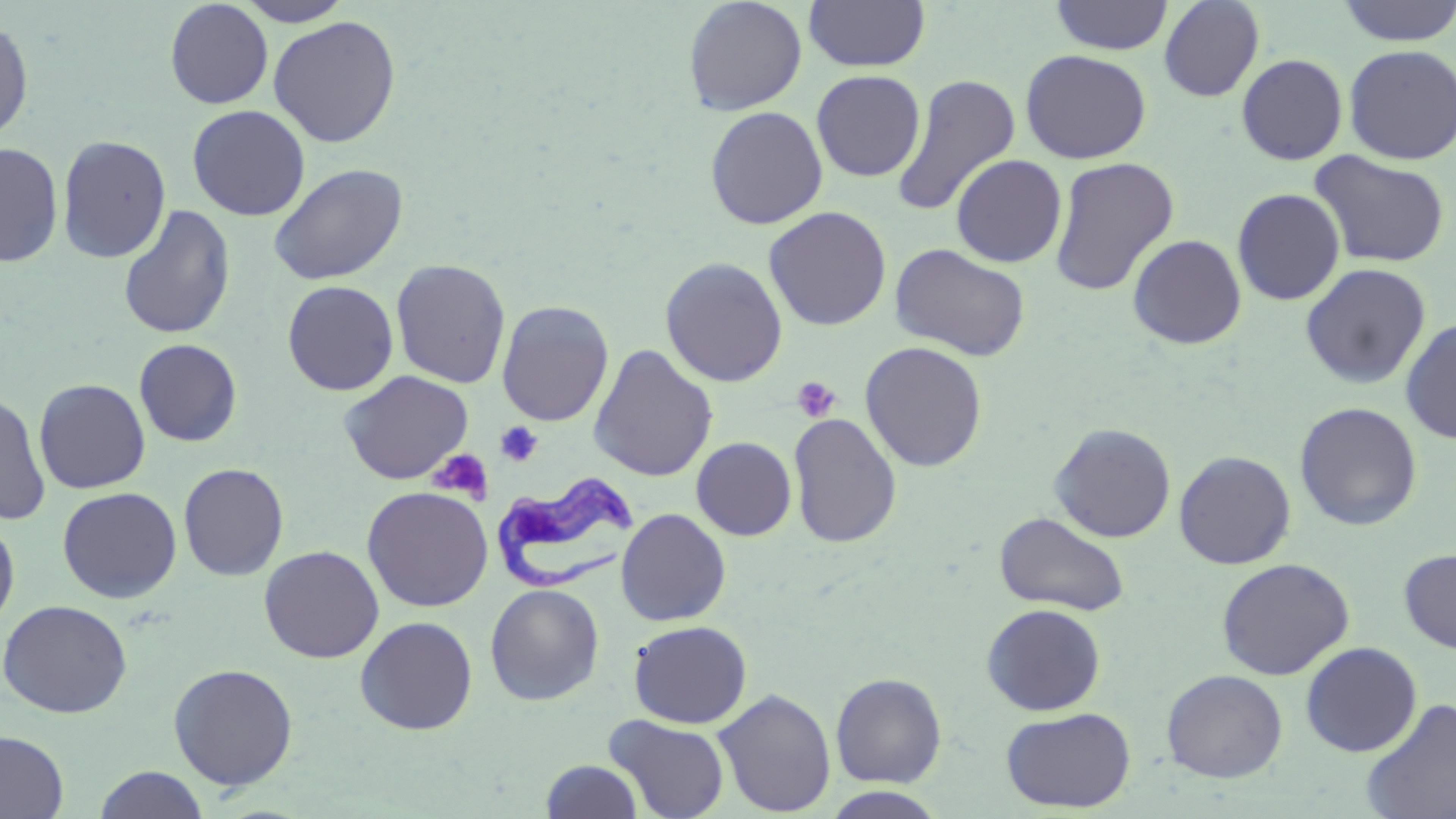

Summary:
  - Coordinate format: approximate bounding boxes as (x1,y1)-(x2,y2) corner pairs in pixels
  - Trypanosoma brucei locations: (490,469)-(639,593)
  - Uninfected red blood cell locations: (236,0)-(354,26), (683,0)-(807,116), (803,0)-(930,72), (1050,0)-(1174,56), (1158,0)-(1265,102), (1335,0)-(1456,47), (165,1)-(273,109), (268,15)-(401,148), (0,16)-(34,144), (1343,43)-(1456,165), (1020,49)-(1152,163), (1236,53)-(1348,165), (811,70)-(925,182), (892,73)-(1020,217), (187,105)-(311,221), (705,105)-(828,230), (57,134)-(171,263), (0,142)-(63,268), (1309,151)-(1451,268), (951,154)-(1067,267), (1049,157)-(1179,296), (269,163)-(408,286), (1232,188)-(1345,305), (117,205)-(235,341), (764,206)-(892,331), (1127,233)-(1247,349), (889,243)-(1030,361), (660,257)-(788,387), (391,259)-(511,388), (1300,263)-(1431,389), (282,280)-(399,396), (497,300)-(614,426), (1400,317)-(1456,444), (133,339)-(242,447), (860,341)-(988,472), (588,344)-(719,482), (339,370)-(473,485), (34,378)-(151,494), (0,391)-(51,525), (1294,402)-(1422,531), (788,412)-(902,548), (1049,422)-(1176,542), (692,437)-(796,540), (1174,450)-(1296,569), (178,462)-(289,581), (362,486)-(493,611), (57,487)-(182,603), (615,508)-(731,626), (994,512)-(1130,617), (0,517)-(20,634), (259,545)-(384,663), (1399,547)-(1456,653), (1216,557)-(1354,680), (485,583)-(605,705), (0,599)-(133,718), (981,603)-(1106,715), (355,616)-(477,735), (628,620)-(752,728), (1300,642)-(1422,757), (168,662)-(298,791), (1162,669)-(1288,782), (830,672)-(947,788), (713,688)-(836,817), (1360,698)-(1456,819), (1001,707)-(1136,813), (604,715)-(730,819), (0,730)-(69,818), (541,759)-(644,818), (93,766)-(210,819), (823,787)-(949,819)
  - Platelet locations: (792,376)-(841,423), (495,421)-(543,467), (428,449)-(494,504)
  - Slide-level diagnosis: Trypanosoma brucei
  - Stain: May-Grünwald-Giemsa
  - Modality: light microscopy
  - Magnification: 1000x
  - Image size: 1456×819 pixels
  - Field of view: one of a larger specimen
  - Preparation: thin blood smear